Describe the morphology of the erythrocytes.
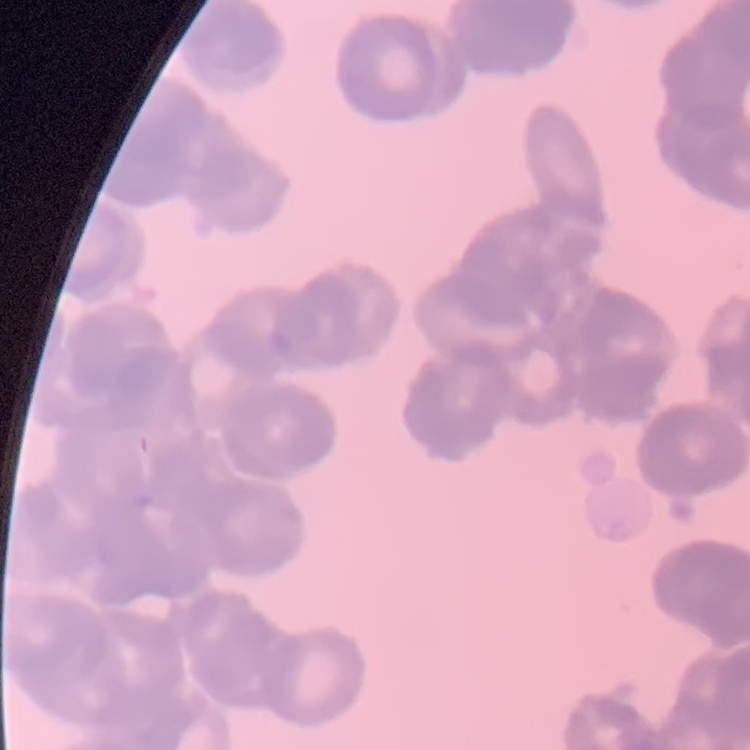

Rouleaux formation.

Field's or Giemsa stain. One tile cut from a larger photomicrograph. Thin peripheral smear.